Outline each blood parasite and name the species.
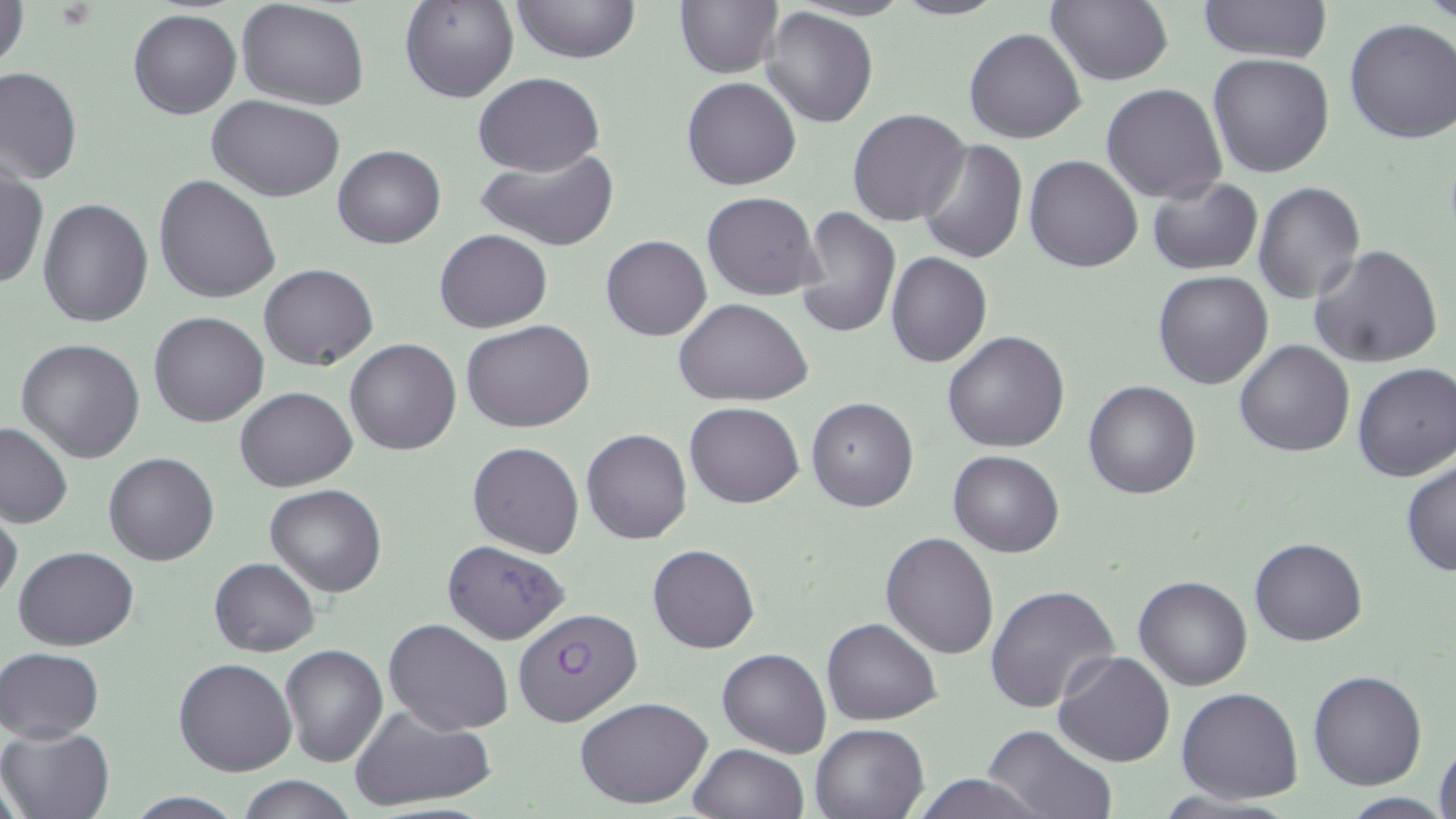

Approximate bounding boxes as named x1/y1/x2/y2 corners in pixels.
Plasmodium falciparum-infected red blood cells: (x1=512, y1=606, x2=642, y2=725).
No Plasmodium ovale, Plasmodium malariae, Plasmodium vivax, Babesia divergens, or Trypanosoma brucei observed.

slide-level diagnosis = Plasmodium falciparum
field of view = one of a larger specimen
modality = optical microscopy
image size = 1456×819 pixels
uninfected red blood cell locations = approximate bounding boxes as named x1/y1/x2/y2 corners in pixels: (x1=399, y1=0, x2=520, y2=104), (x1=511, y1=0, x2=640, y2=65), (x1=675, y1=0, x2=783, y2=79), (x1=892, y1=0, x2=1007, y2=21), (x1=1197, y1=0, x2=1333, y2=66), (x1=1421, y1=0, x2=1454, y2=30), (x1=1046, y1=1, x2=1173, y2=87), (x1=1, y1=2, x2=29, y2=74), (x1=237, y1=2, x2=368, y2=109), (x1=761, y1=6, x2=878, y2=127), (x1=127, y1=9, x2=241, y2=119), (x1=1343, y1=18, x2=1456, y2=144), (x1=965, y1=29, x2=1085, y2=145), (x1=1206, y1=53, x2=1335, y2=178), (x1=0, y1=66, x2=82, y2=186), (x1=472, y1=71, x2=604, y2=175), (x1=681, y1=77, x2=801, y2=190), (x1=1102, y1=83, x2=1228, y2=204), (x1=208, y1=96, x2=346, y2=201), (x1=846, y1=108, x2=971, y2=228), (x1=918, y1=140, x2=1028, y2=265), (x1=333, y1=144, x2=445, y2=249), (x1=475, y1=147, x2=621, y2=251), (x1=1025, y1=155, x2=1144, y2=272), (x1=0, y1=168, x2=48, y2=291), (x1=153, y1=174, x2=281, y2=304), (x1=1147, y1=177, x2=1263, y2=276), (x1=1253, y1=181, x2=1364, y2=304), (x1=702, y1=192, x2=822, y2=300), (x1=37, y1=198, x2=153, y2=328), (x1=797, y1=207, x2=900, y2=338), (x1=434, y1=229, x2=551, y2=333), (x1=601, y1=235, x2=711, y2=341), (x1=1307, y1=244, x2=1444, y2=369), (x1=886, y1=252, x2=992, y2=367), (x1=258, y1=263, x2=379, y2=369), (x1=1152, y1=269, x2=1273, y2=388), (x1=673, y1=298, x2=813, y2=407), (x1=150, y1=311, x2=269, y2=427), (x1=462, y1=319, x2=594, y2=433), (x1=942, y1=330, x2=1070, y2=452), (x1=15, y1=338, x2=146, y2=463), (x1=346, y1=338, x2=462, y2=455), (x1=1234, y1=339, x2=1356, y2=456), (x1=1352, y1=361, x2=1456, y2=482), (x1=1083, y1=380, x2=1201, y2=498), (x1=235, y1=387, x2=357, y2=492), (x1=806, y1=396, x2=919, y2=512), (x1=685, y1=401, x2=804, y2=508), (x1=0, y1=420, x2=75, y2=528), (x1=581, y1=428, x2=692, y2=544), (x1=467, y1=441, x2=585, y2=559), (x1=948, y1=450, x2=1064, y2=557), (x1=105, y1=452, x2=219, y2=565), (x1=1400, y1=460, x2=1456, y2=577), (x1=264, y1=484, x2=387, y2=596), (x1=0, y1=504, x2=23, y2=606), (x1=880, y1=532, x2=1000, y2=659), (x1=1249, y1=536, x2=1368, y2=646), (x1=441, y1=539, x2=570, y2=644), (x1=647, y1=543, x2=760, y2=654), (x1=13, y1=544, x2=139, y2=650), (x1=208, y1=557, x2=319, y2=656), (x1=1134, y1=576, x2=1253, y2=690), (x1=985, y1=584, x2=1121, y2=716), (x1=822, y1=616, x2=941, y2=725), (x1=384, y1=618, x2=513, y2=735), (x1=279, y1=645, x2=388, y2=767), (x1=1, y1=647, x2=103, y2=742), (x1=718, y1=647, x2=831, y2=757), (x1=1052, y1=650, x2=1177, y2=767), (x1=174, y1=656, x2=297, y2=777), (x1=1308, y1=670, x2=1428, y2=790), (x1=1177, y1=687, x2=1304, y2=804), (x1=574, y1=696, x2=714, y2=808), (x1=351, y1=706, x2=497, y2=812), (x1=808, y1=721, x2=930, y2=818), (x1=980, y1=725, x2=1117, y2=819), (x1=2, y1=726, x2=113, y2=819), (x1=1433, y1=740, x2=1455, y2=816), (x1=689, y1=743, x2=808, y2=819), (x1=907, y1=774, x2=1051, y2=818), (x1=240, y1=775, x2=357, y2=819), (x1=1340, y1=794, x2=1452, y2=818)
preparation = thin blood smear
magnification = 1000x
stain = May-Grünwald-Giemsa